Give the position of every leukocyte visible.
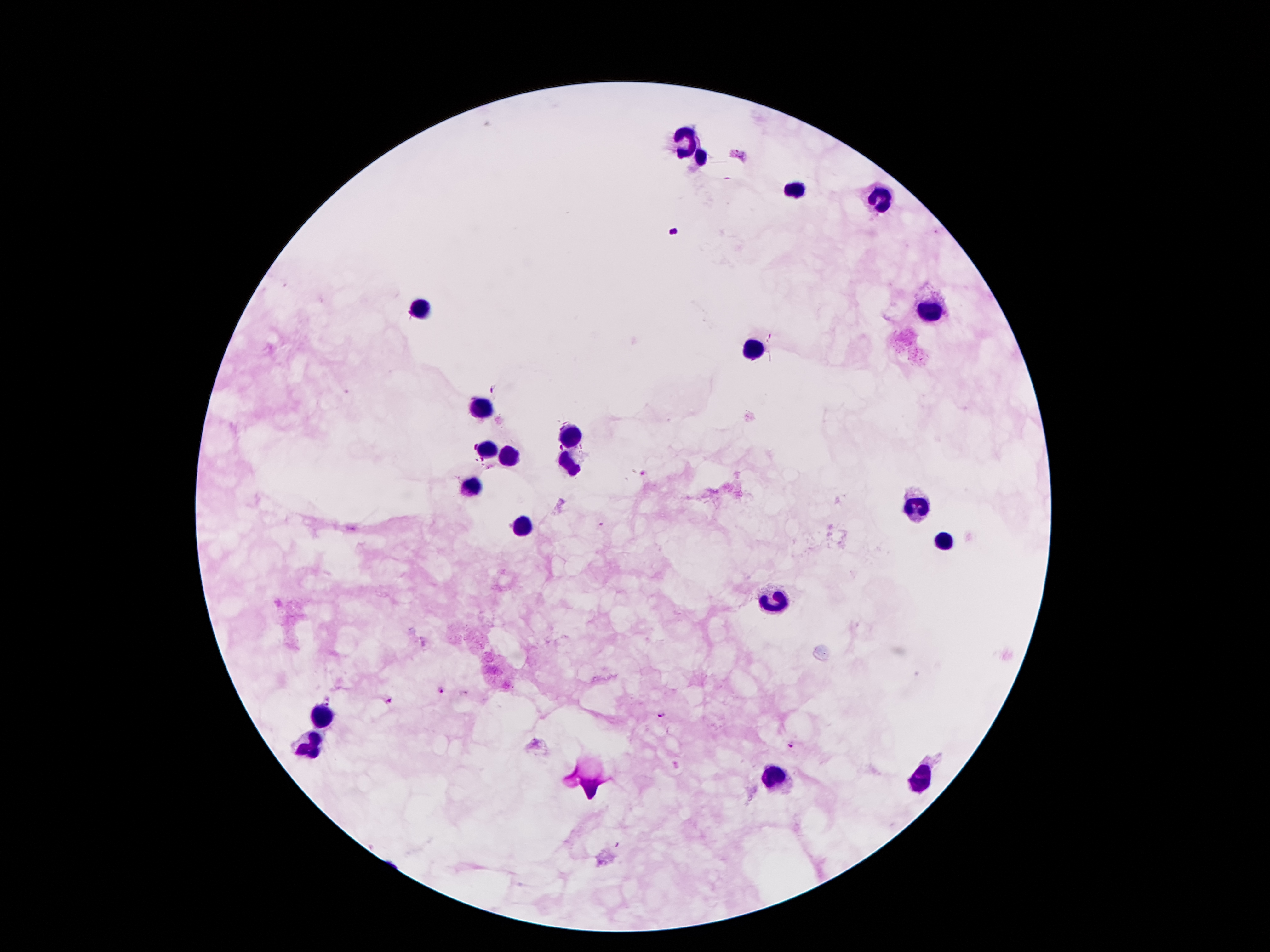
Approximate centers as {x, y} in pixels.
Leukocytes: {685, 138}, {701, 159}, {795, 190}, {881, 200}, {419, 310}, {931, 314}, {752, 353}, {479, 409}, {569, 435}, {490, 450}, {509, 455}, {569, 465}, {470, 485}, {916, 504}, {522, 528}, {942, 541}, {778, 603}, {320, 720}, {311, 745}, {776, 780}, {920, 780}.

Summary:
  - Plasmodium parasite locations: {739, 156}, {496, 388}, {645, 474}, {440, 691}, {390, 700}, {663, 716}, {790, 745}
  - Preparation: thick peripheral-blood smear
  - Stain: Giemsa
  - Field of view: one from this slide
  - Patient malaria status: infected with Plasmodium falciparum
  - Capture: smartphone through the microscope eyepiece
  - Image size: 1270×952 pixels
  - Magnification: 100x